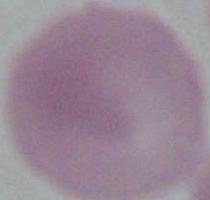

modality = micrograph
identification = erythrocyte
magnification = 1000x